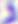 Captured at 400x magnification. Toxoplasma gondii is shown. Micrograph.